Outline each blood parasite and name the species.
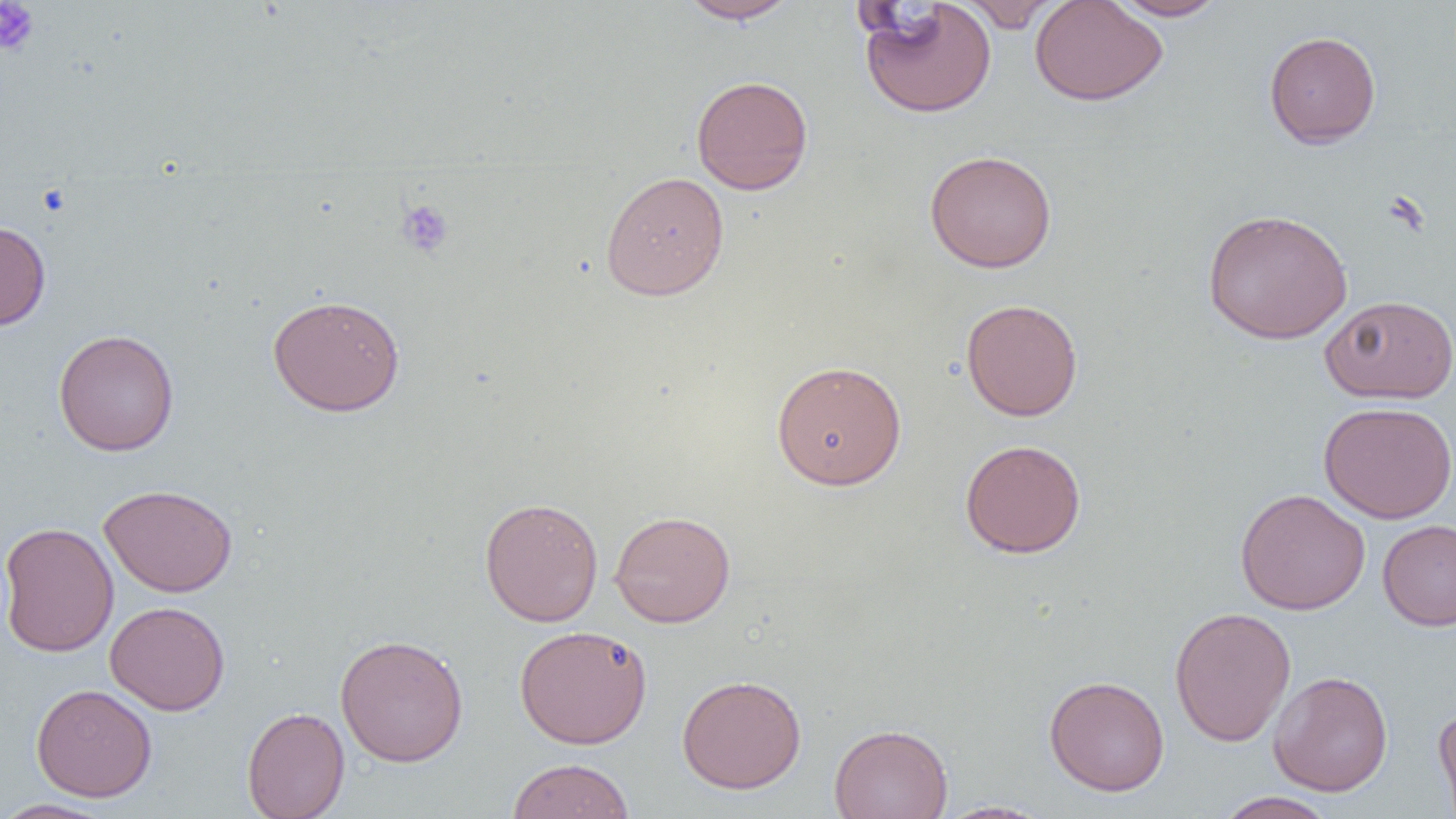
No blood parasites seen.

Summary:
  - Coordinate format: approximate bounding boxes as [x1, y1, x2, y2] in pixels
  - Platelet locations: [0, 0, 39, 57], [38, 184, 71, 216], [396, 199, 455, 258]
  - Uninfected red blood cell locations: [677, 0, 801, 24], [857, 0, 997, 118], [959, 0, 1063, 32], [1029, 0, 1168, 106], [1108, 0, 1229, 21], [1264, 30, 1381, 148], [690, 75, 814, 195], [924, 149, 1057, 273], [600, 171, 729, 300], [1202, 208, 1353, 345], [0, 220, 51, 330], [267, 294, 405, 417], [1321, 294, 1456, 404], [961, 298, 1083, 421], [53, 329, 179, 456], [771, 359, 907, 491], [1318, 401, 1456, 524], [959, 439, 1086, 559], [98, 483, 238, 597], [1235, 488, 1370, 615], [479, 497, 603, 626], [609, 510, 736, 628], [1377, 518, 1456, 631], [0, 522, 118, 657], [105, 600, 230, 716], [1169, 606, 1296, 747], [514, 624, 653, 748], [335, 634, 469, 766], [1268, 670, 1393, 796], [677, 674, 806, 794], [1044, 675, 1170, 796], [31, 684, 157, 802], [1433, 705, 1456, 819], [242, 706, 350, 819], [829, 723, 953, 819], [507, 758, 635, 819], [1215, 791, 1339, 819], [0, 798, 117, 818], [933, 800, 1053, 818]
  - Slide-level diagnosis: no evidence of blood parasites
  - Image size: 1456×819 pixels
  - Modality: light microscopy
  - Preparation: thin blood film
  - Field of view: one of a larger specimen
  - Magnification: 1000x